Classify this cell by malaria status.
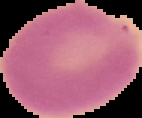
It is uninfected.

From a thin blood smear. The area outside the segmented cell region is set to black. Image is 142×118 pixels.